Point out each malaria parasite.
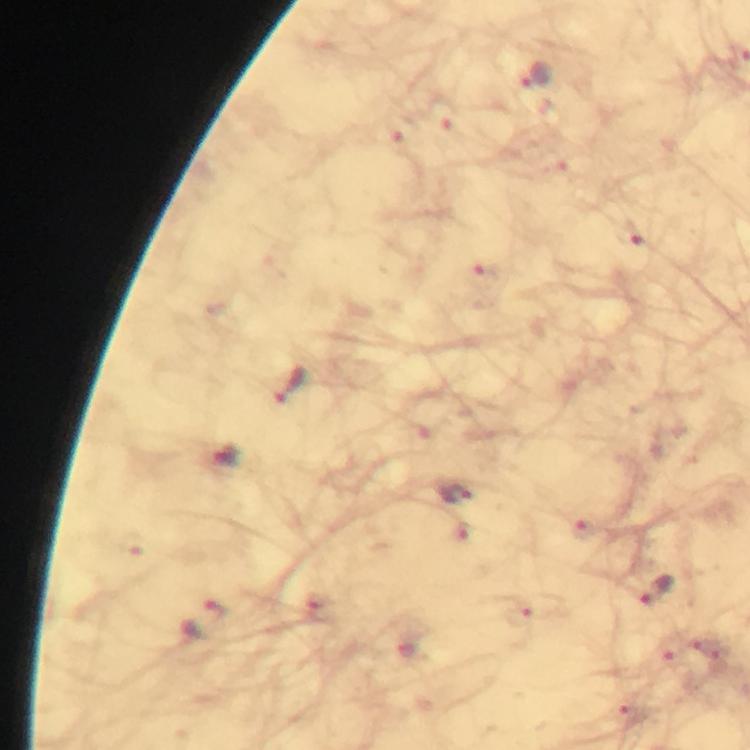
Approximate centers as (x, y) in pixels.
Malaria parasites: (537, 80), (290, 386), (224, 459), (454, 497), (659, 591), (205, 619).

From a malaria diagnostic workup. 100x magnification. Image is 750×750 pixels. Immersion oil applied. Cropped region of a single field of view. Giemsa stain. Photographed through the microscope with a smartphone camera. Thick smear.